Give the extent of all Trypanosoma brucei.
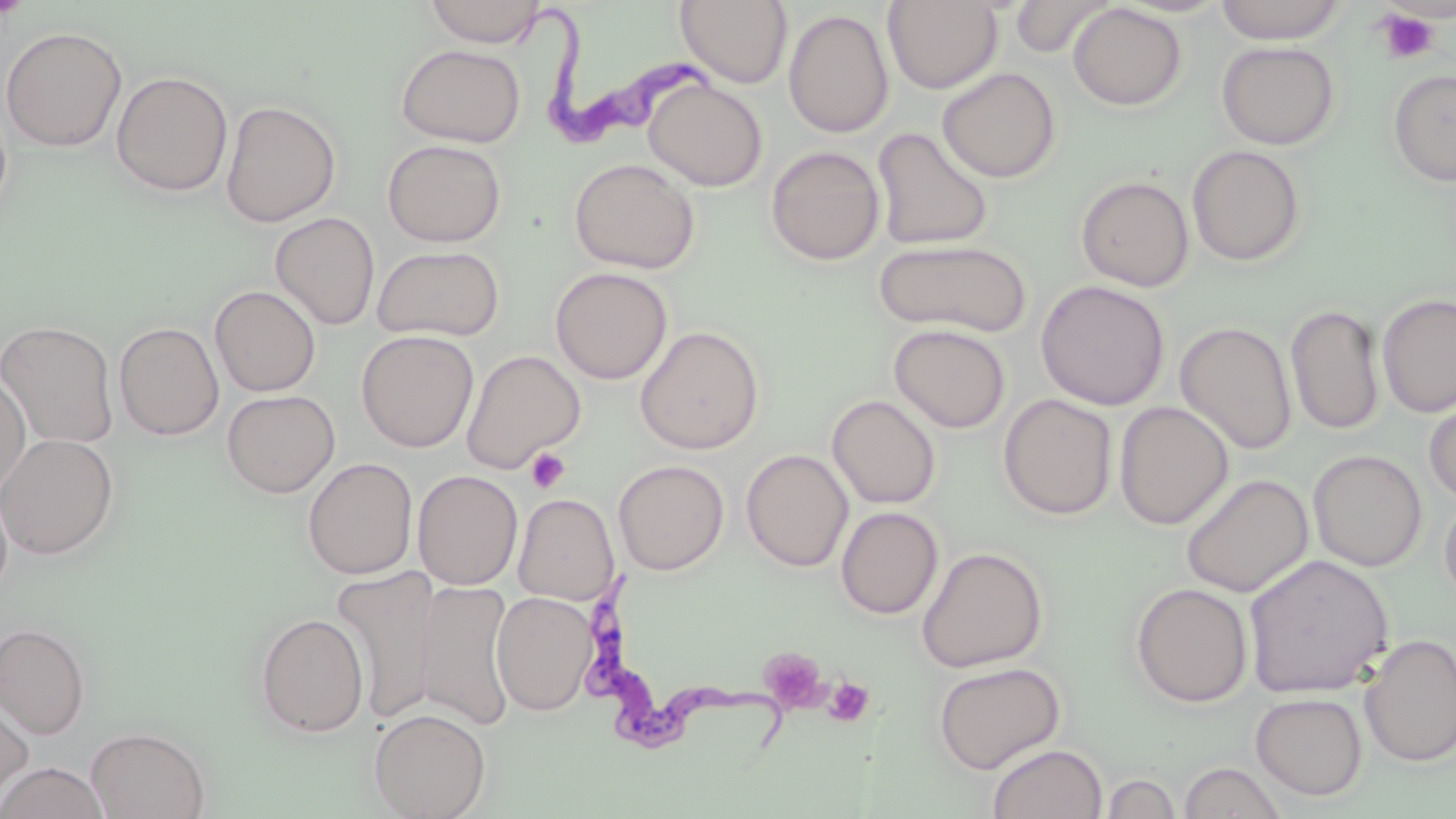

Approximate bounding boxes as (x1, y1, x2, y2) in pixels.
Trypanosoma brucei: (539, 16, 710, 154), (583, 568, 790, 773).

slide-level diagnosis = Trypanosoma brucei
magnification = 1000x
image size = 1456×819 pixels
platelet locations = approximate bounding boxes as (x1, y1, x2, y2) in pixels: (1375, 8, 1442, 65), (526, 448, 570, 493), (758, 647, 828, 712), (822, 676, 875, 728)
stain = May-Grünwald-Giemsa
preparation = thin blood film
field of view = one of a larger specimen
modality = light microscopy
uninfected red blood cell locations = approximate bounding boxes as (x1, y1, x2, y2) in pixels: (424, 0, 547, 47), (675, 0, 793, 88), (1009, 0, 1115, 58), (882, 1, 1002, 94), (1214, 1, 1349, 45), (1067, 3, 1187, 111), (783, 9, 894, 138), (0, 26, 127, 153), (1216, 40, 1340, 150), (395, 43, 526, 147), (937, 67, 1061, 183), (1387, 68, 1456, 188), (111, 71, 233, 197), (643, 79, 767, 192), (0, 96, 13, 226), (220, 99, 342, 227), (871, 127, 994, 250), (382, 139, 507, 247), (766, 145, 885, 266), (1187, 145, 1306, 267), (569, 158, 700, 274), (1075, 175, 1195, 292), (270, 212, 380, 331), (874, 239, 1032, 337), (371, 245, 505, 342), (550, 267, 673, 384), (1035, 279, 1170, 411), (210, 286, 321, 397), (1377, 292, 1456, 418), (1286, 303, 1385, 435), (0, 320, 119, 449), (1175, 321, 1297, 455), (114, 322, 224, 440), (889, 324, 1011, 433), (635, 325, 765, 455), (356, 330, 479, 452), (461, 349, 585, 474), (0, 371, 31, 497), (221, 389, 340, 497), (1423, 393, 1456, 504), (827, 394, 942, 509), (998, 394, 1118, 520), (1114, 401, 1233, 530), (0, 433, 119, 560), (741, 449, 853, 572), (1307, 449, 1428, 572), (303, 457, 418, 579), (613, 459, 729, 575), (412, 470, 523, 590), (1180, 473, 1313, 598), (0, 481, 14, 602), (1439, 491, 1456, 611), (513, 493, 619, 604), (835, 506, 943, 619), (916, 546, 1049, 673), (1243, 553, 1395, 699), (331, 567, 442, 725), (416, 581, 516, 728), (1130, 582, 1253, 708), (491, 591, 596, 716), (254, 612, 369, 739), (0, 623, 90, 740), (1359, 633, 1456, 768), (933, 661, 1066, 775), (1250, 692, 1368, 801), (0, 698, 34, 808), (369, 708, 491, 819), (87, 726, 211, 819), (987, 743, 1107, 819), (1177, 760, 1289, 818), (1, 762, 109, 819), (1099, 772, 1182, 818)